Report the malaria status of this cell.
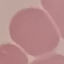

Uninfected.

Summary:
  - Preparation: thin smear
  - Image type: cell patch, automatically extracted from a larger field of view and resized to 64 × 64 pixels
  - Stain: Giemsa
  - Capture: smartphone through the microscope eyepiece